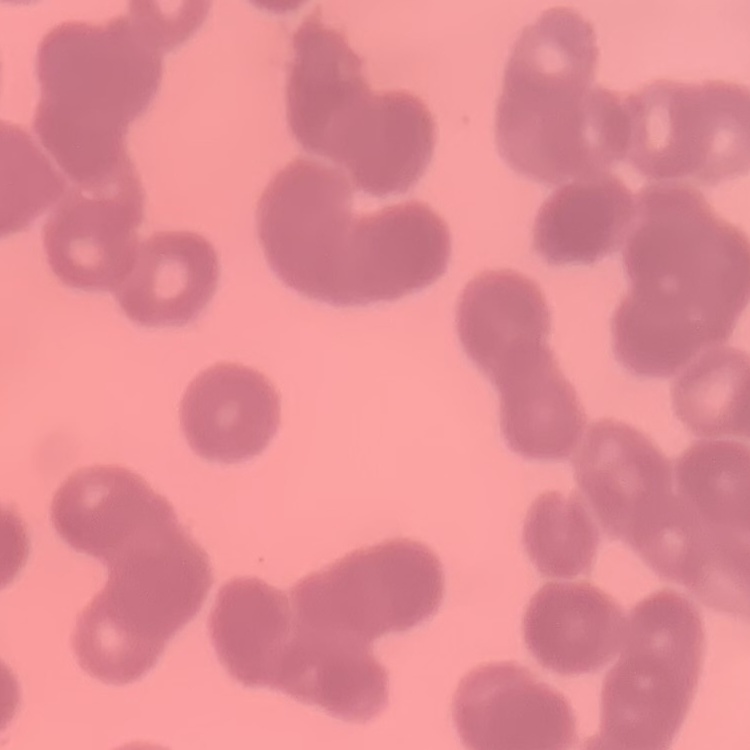

Summary:
  - Erythrocyte morphology: rouleaux formation
  - Stain: Field's or Giemsa
  - Image type: square crop of a larger photomicrograph
  - Preparation: thin blood film